Locate every blood parasite and identify its species.
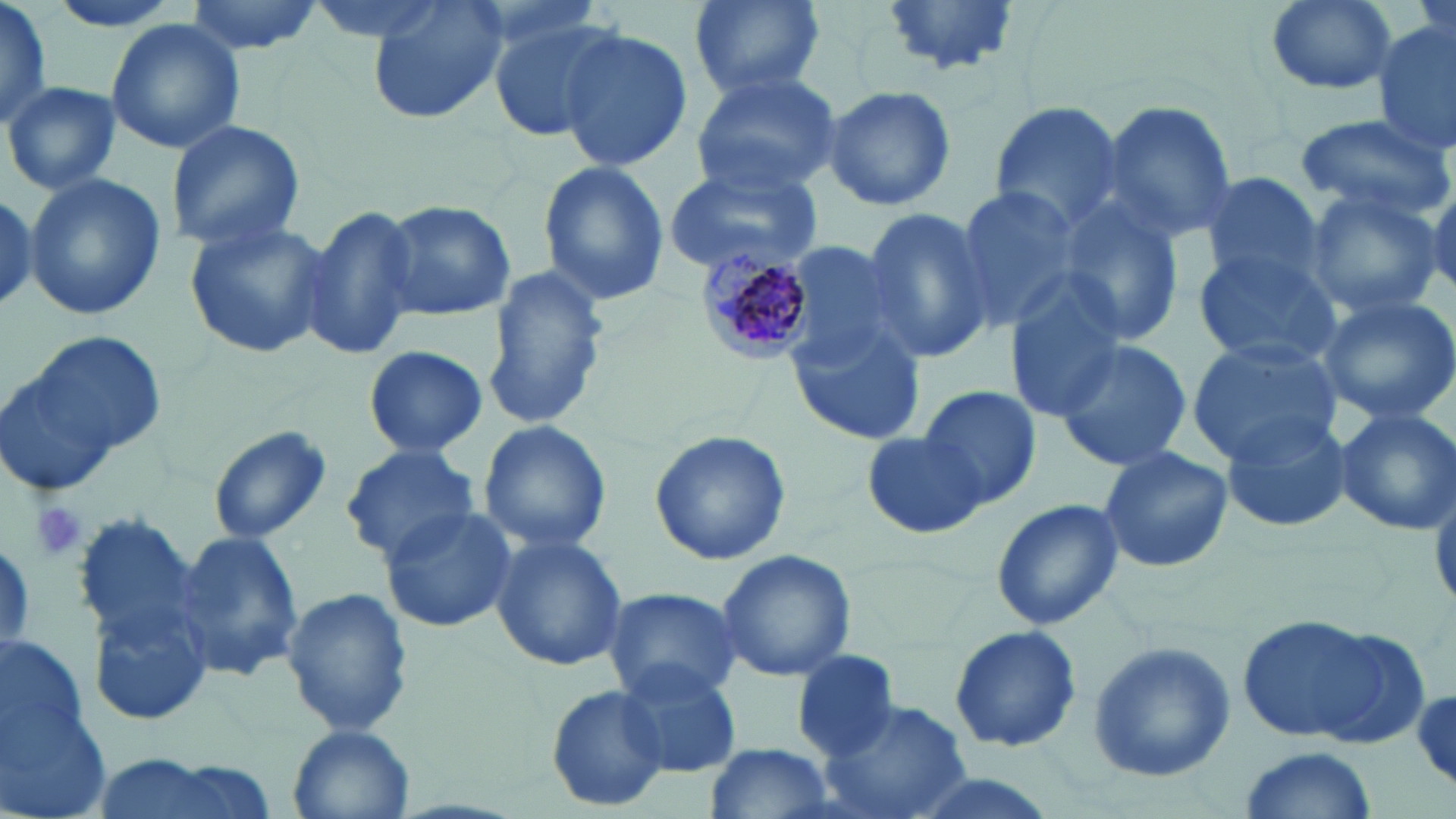

Approximate bounding boxes as [x1, y1, x2, y2] in pixels.
Plasmodium malariae-infected red blood cells: [695, 247, 818, 363].
No Plasmodium falciparum, Plasmodium ovale, Plasmodium vivax, Babesia divergens, or Trypanosoma brucei observed.

Summary:
  - Uninfected red blood cell locations: [47, 0, 185, 34], [184, 0, 325, 56], [303, 0, 461, 43], [366, 0, 508, 125], [685, 0, 828, 100], [877, 0, 1026, 77], [1261, 0, 1397, 97], [0, 2, 51, 128], [486, 10, 623, 142], [105, 18, 245, 156], [1373, 18, 1455, 159], [554, 27, 694, 174], [687, 69, 843, 194], [4, 81, 120, 194], [823, 85, 956, 212], [1098, 98, 1239, 246], [986, 101, 1129, 235], [1294, 112, 1452, 220], [165, 120, 304, 250], [661, 160, 825, 276], [537, 161, 669, 306], [1202, 172, 1324, 288], [26, 173, 166, 322], [948, 186, 1080, 330], [1304, 186, 1446, 319], [0, 189, 38, 310], [301, 200, 421, 364], [378, 201, 515, 320], [1049, 201, 1186, 347], [861, 208, 996, 366], [182, 220, 334, 361], [773, 241, 922, 371], [1193, 249, 1340, 367], [483, 264, 610, 430], [1003, 282, 1131, 421], [1314, 292, 1456, 425], [785, 317, 925, 445], [0, 331, 162, 493], [1185, 335, 1345, 465], [1052, 338, 1194, 471], [363, 345, 487, 457], [916, 385, 1043, 511], [1332, 407, 1456, 535], [1223, 409, 1357, 533], [479, 419, 611, 556], [209, 426, 329, 547], [650, 428, 789, 565], [864, 429, 988, 539], [340, 444, 481, 563], [1097, 446, 1234, 573], [989, 496, 1125, 631], [377, 503, 518, 633], [75, 508, 219, 718], [173, 529, 304, 684], [488, 532, 629, 672], [716, 548, 856, 683], [603, 586, 743, 703], [283, 587, 411, 738], [1236, 614, 1423, 748], [949, 624, 1082, 753], [0, 633, 87, 762], [1086, 638, 1236, 781], [790, 650, 899, 761], [614, 661, 742, 777], [547, 686, 668, 809], [1411, 688, 1454, 787], [821, 698, 973, 819], [0, 703, 114, 819], [288, 725, 415, 819], [702, 742, 837, 819], [1237, 747, 1378, 818]
  - Platelet locations: [30, 501, 86, 561]
  - Slide-level diagnosis: Plasmodium malariae
  - Modality: optical microscopy
  - Stain: May-Grünwald-Giemsa
  - Magnification: 1000x
  - Image size: 1456×819 pixels
  - Preparation: thin blood film
  - Field of view: one of a larger specimen